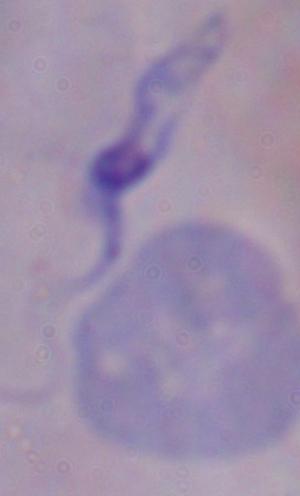

{
  "magnification": "1000x",
  "modality": "micrograph",
  "identification": "trypanosome"
}